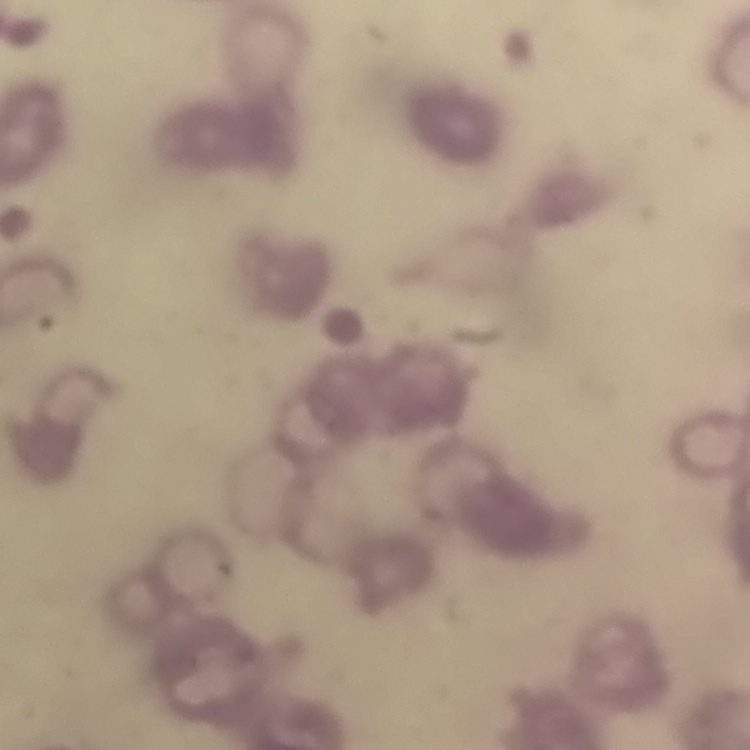
The red blood cells show rouleaux formation. Square crop of a larger photomicrograph. Stained with either Field's or Giemsa. Thin blood film.